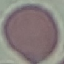
{
  "malaria_status": "uninfected",
  "preparation": "thin blood film",
  "image_type": "cell patch, automatically extracted from a larger field of view and resized to 64 × 64 pixels",
  "stain": "Giemsa",
  "capture": "smartphone through the microscope eyepiece"
}